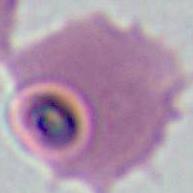

Photomicrograph. A Plasmodium parasite is seen. Captured at either 400x or 1000x magnification.